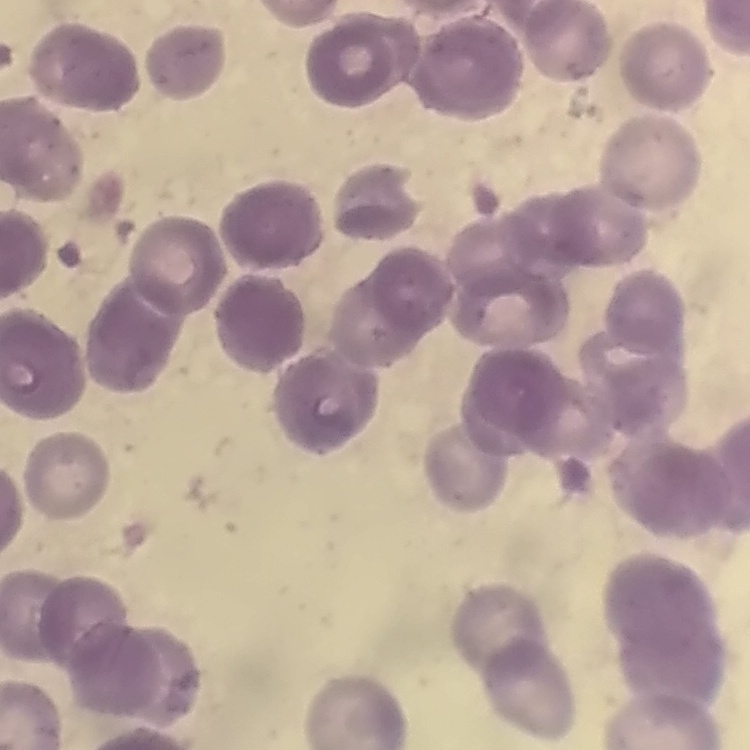

erythrocyte_morphology: rouleaux formation
stain: Field's or Giemsa
image_type: one tile cut from a larger photomicrograph
preparation: thin blood film